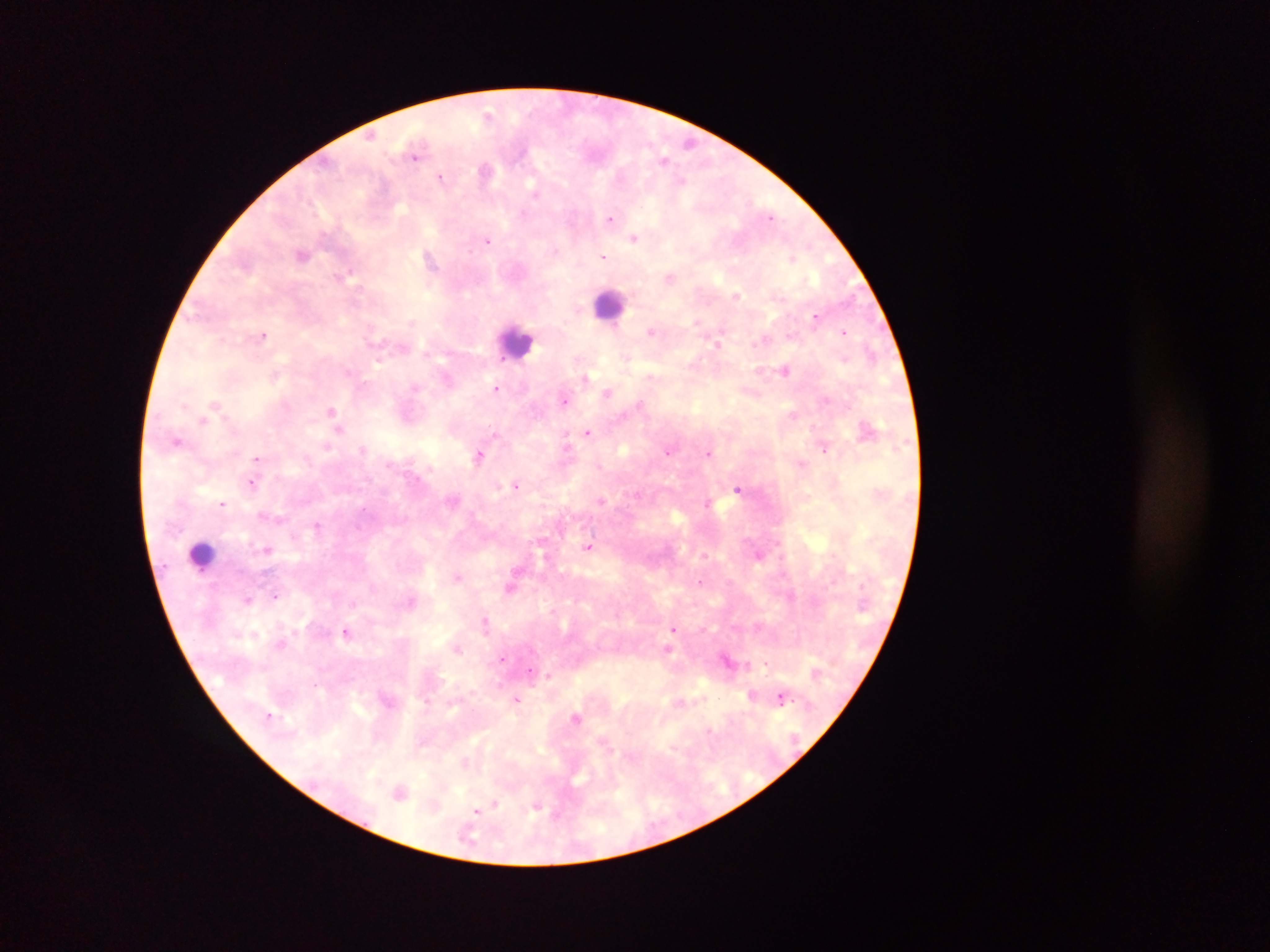

country: Ghana
field_of_view: single
capture: mobile-phone photograph through a microscope
plasmodium_parasite_locations: 'approximate centers as x y in pixels: 416 158; 440 178; 611 217; 772 217; 488 241; 604 256; 815 316; 844 330; 265 337; 496 387; 564 400; 588 432; 823 447; 669 452; 709 452; 479 457; 258 458; 251 482; 516 485; 738 489; 601 501; 709 503; 221 504; 590 547; 701 582; 274 594; 672 628; 347 633; 503 659; 767 662; 313 685; 780 694; 478 811'
preparation: thick blood smear
leukocyte_locations: 'approximate centers as x y in pixels: 605 306; 517 336; 203 557'
image_size: 1270×952 pixels